Locate every blood parasite and identify its species.
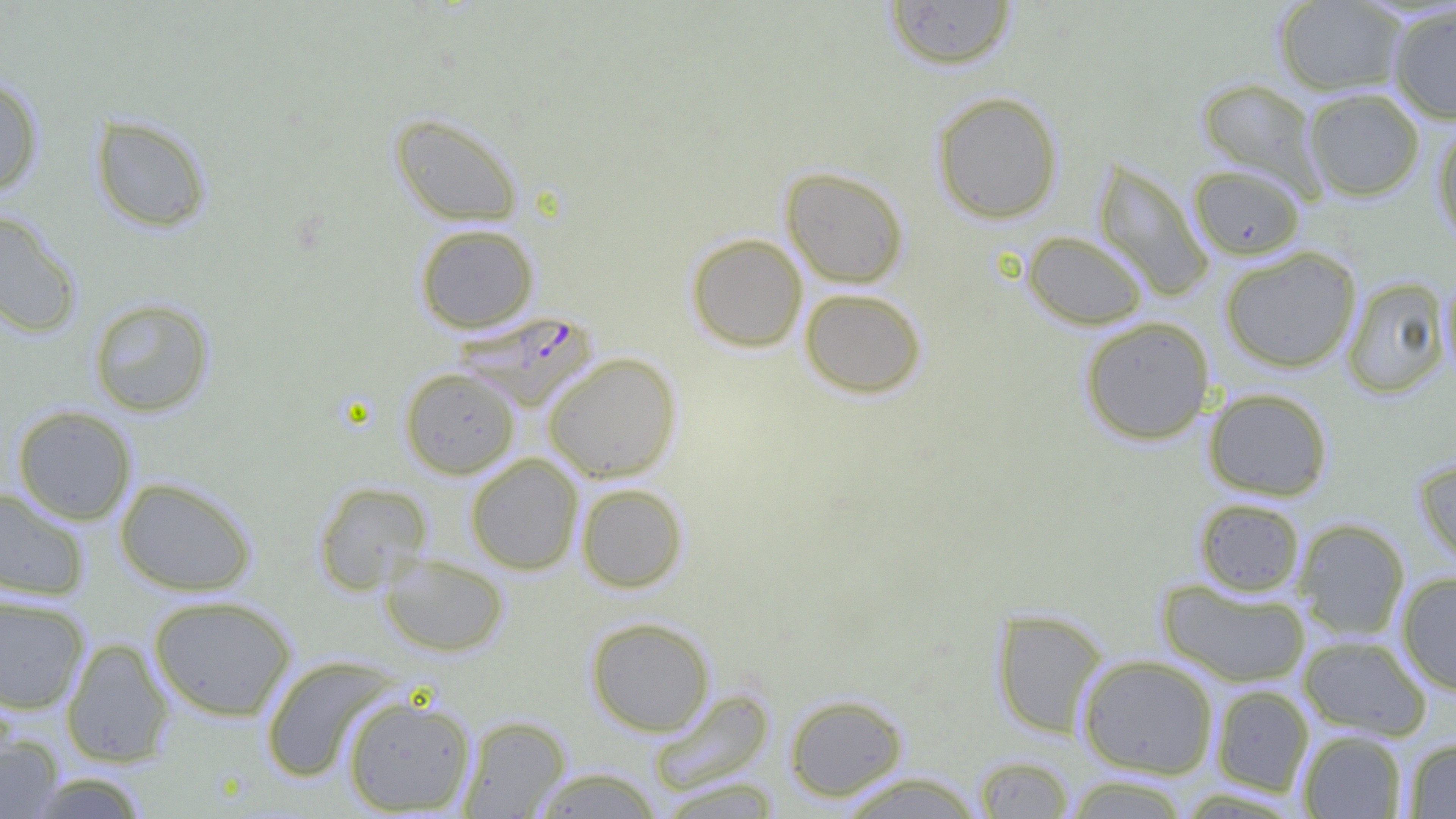
Approximate bounding boxes as (x1,y1)-(x2,y2) corner pairs in pixels.
Plasmodium falciparum-infected red blood cells: (452,310)-(598,411).
No Plasmodium ovale, Plasmodium malariae, Plasmodium vivax, Babesia divergens, or Trypanosoma brucei observed.

Uninfected red blood cell locations: (1273,0)-(1408,96), (883,1)-(1017,71), (1387,4)-(1456,124), (0,74)-(44,197), (1197,78)-(1323,195), (1303,87)-(1425,201), (931,90)-(1063,224), (389,112)-(524,227), (90,114)-(212,233), (1432,120)-(1456,247), (1093,158)-(1214,302), (1189,165)-(1305,260), (781,166)-(909,288), (0,209)-(82,339), (414,223)-(539,333), (1022,231)-(1149,330), (686,232)-(808,352), (1220,246)-(1361,373), (1441,274)-(1456,383), (1341,277)-(1451,398), (799,288)-(927,399), (88,296)-(215,417), (1079,316)-(1215,445), (543,352)-(682,483), (400,367)-(520,479), (1203,387)-(1333,501), (12,405)-(137,526), (465,453)-(583,574), (1414,456)-(1456,567), (115,475)-(257,596), (313,480)-(432,594), (576,483)-(688,592), (0,488)-(90,602), (1194,497)-(1305,597), (1293,518)-(1410,641), (379,553)-(509,657), (1396,571)-(1456,695), (1157,578)-(1310,688), (0,593)-(91,715), (148,595)-(297,722), (991,607)-(1109,738), (585,616)-(715,736), (1298,634)-(1432,740), (61,637)-(175,767), (1077,654)-(1218,778), (260,655)-(403,783), (1210,684)-(1314,797), (649,688)-(775,795), (341,693)-(477,815), (784,693)-(908,802), (458,715)-(571,818), (1297,730)-(1408,818), (0,734)-(65,818), (1403,737)-(1456,818), (974,755)-(1075,818), (528,766)-(664,818), (834,771)-(987,818), (22,772)-(152,818), (1060,775)-(1192,818), (653,777)-(786,818). Slide-level diagnosis: Plasmodium falciparum. Thin blood smear. Light microscopy. Captured at 1000x magnification. Image is 1456×819 pixels. One field of a larger specimen.